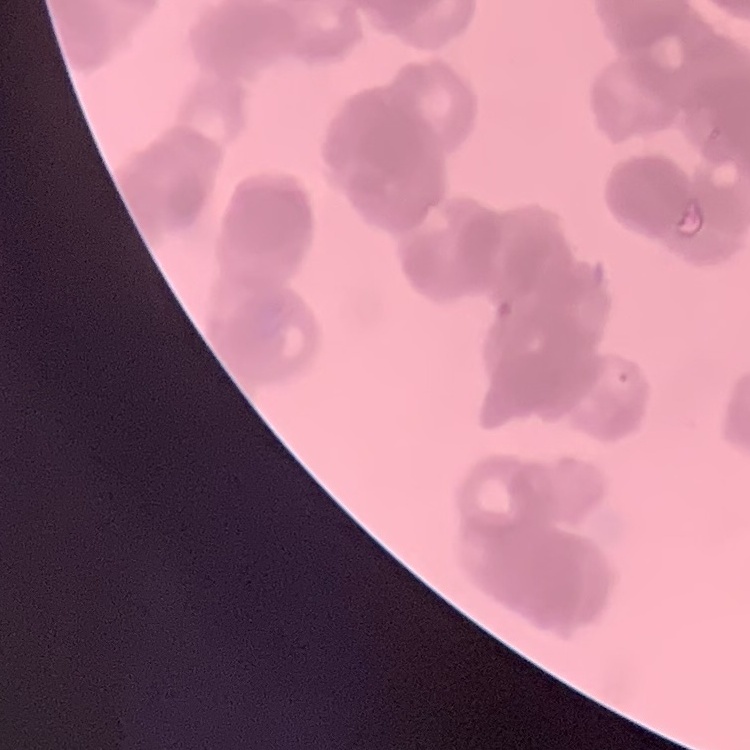
The erythrocytes exhibit rouleaux formation. One tile cut from a larger photomicrograph. Stained with either Field's or Giemsa. Thin blood smear.